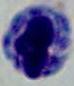
modality = micrograph
magnification = 1000x
identification = leukocyte